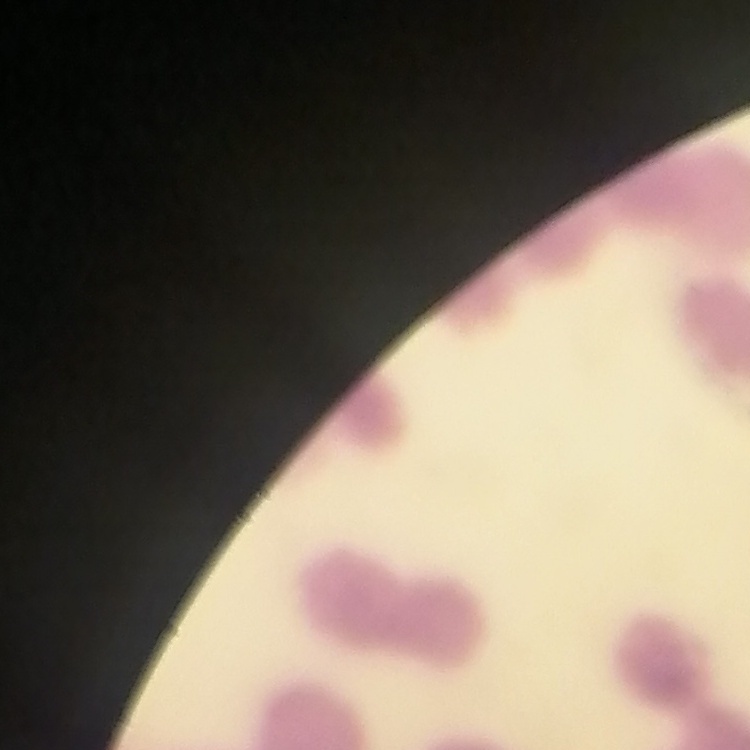

Summary:
  - Erythrocyte morphology: rouleaux formation
  - Preparation: thin blood film
  - Image type: one tile cut from a larger photomicrograph
  - Stain: Field's or Giemsa